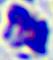

Summary:
  - Identification: white blood cell
  - Magnification: 400x
  - Modality: micrograph